Name the parasite shown.
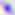
This is Toxoplasma gondii.

Photomicrograph. 400x magnification.